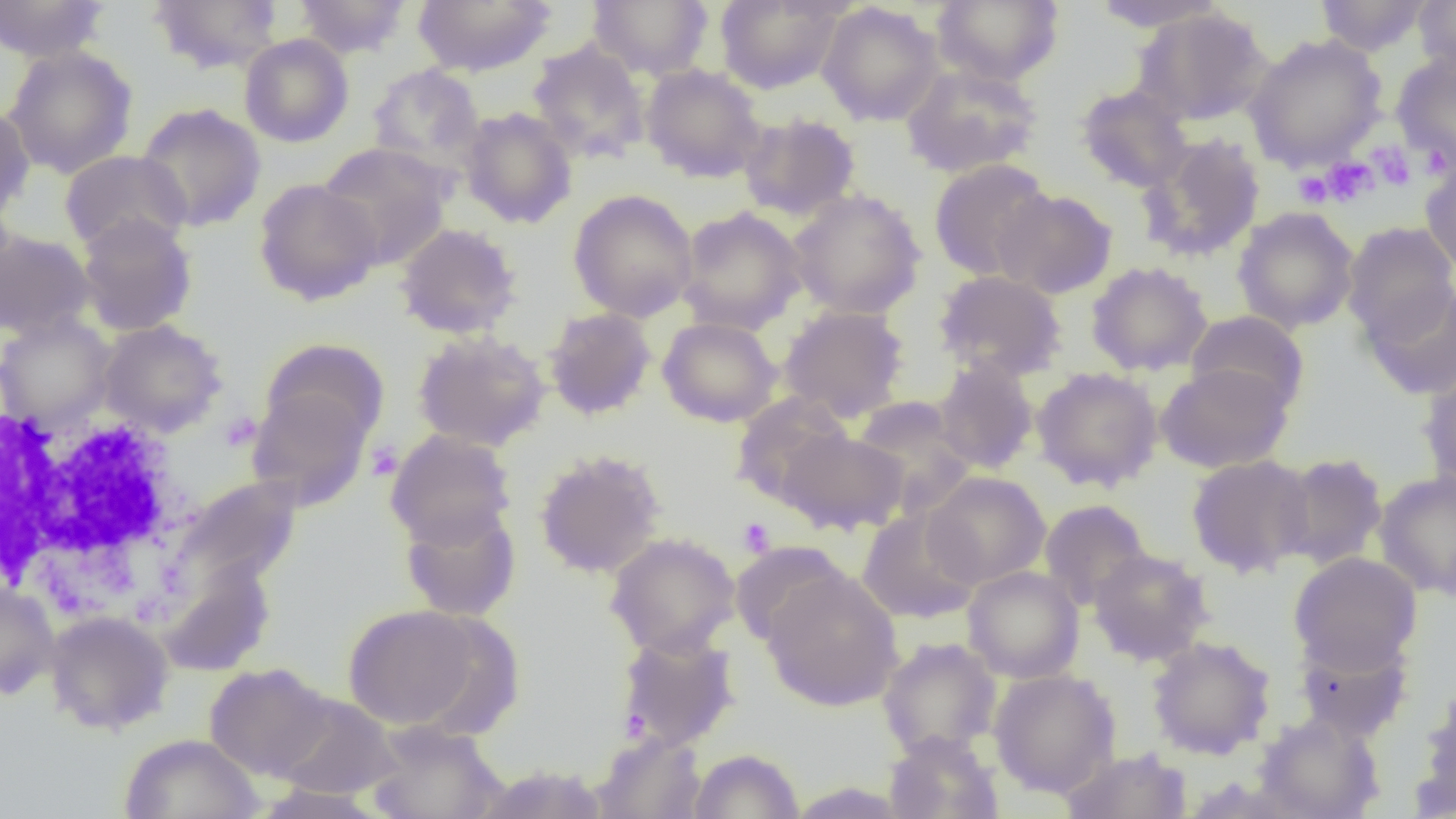

Summary:
  - Coordinate format: approximate bounding boxes as (x1,y1)-(x2,y2) corner pairs in pixels
  - Uninfected red blood cell locations: (0,0)-(110,62), (147,0)-(283,75), (293,0)-(412,59), (413,0)-(556,77), (587,0)-(714,80), (714,0)-(849,95), (931,0)-(1065,86), (1088,0)-(1228,32), (1313,0)-(1434,56), (1414,0)-(1456,79), (816,2)-(945,127), (1133,7)-(1273,127), (239,33)-(354,148), (1244,34)-(1387,171), (527,40)-(651,165), (2,45)-(139,179), (1391,54)-(1456,175), (366,64)-(486,177), (641,64)-(767,183), (900,64)-(1044,178), (1075,84)-(1194,193), (0,100)-(35,222), (135,102)-(267,233), (459,106)-(578,229), (738,113)-(861,220), (1138,133)-(1266,262), (316,142)-(454,270), (59,149)-(191,255), (1420,156)-(1456,277), (928,159)-(1052,281), (253,178)-(382,305), (568,188)-(699,322), (788,188)-(926,320), (992,188)-(1118,299), (676,205)-(807,335), (1232,206)-(1360,334), (75,213)-(198,336), (394,222)-(523,339), (1342,222)-(1456,346), (0,229)-(96,340), (1086,261)-(1213,377), (933,270)-(1067,382), (1362,283)-(1456,400), (778,305)-(910,423), (543,307)-(658,421), (1185,310)-(1309,412), (0,314)-(116,428), (657,316)-(782,427), (97,319)-(227,437), (412,330)-(551,451), (259,338)-(390,451), (932,359)-(1039,474), (1155,363)-(1294,473), (1418,363)-(1456,493), (1031,366)-(1164,492), (246,385)-(374,512), (730,393)-(853,509), (850,396)-(977,514), (384,429)-(517,549), (779,429)-(908,535), (534,448)-(667,580), (1275,452)-(1389,570), (1186,455)-(1314,578), (1374,470)-(1456,599), (923,471)-(1051,588), (171,476)-(303,597), (1039,499)-(1151,610), (399,502)-(522,621), (857,507)-(983,624), (604,532)-(741,659), (1088,547)-(1214,666), (1289,552)-(1422,673), (156,559)-(276,676), (963,565)-(1084,683), (976,566)-(1096,799), (761,568)-(904,712), (0,581)-(60,701), (342,603)-(491,732), (45,610)-(174,734), (614,630)-(742,754), (1293,630)-(1414,742), (1146,635)-(1276,759), (877,637)-(1002,759), (204,662)-(335,780), (988,668)-(1122,798), (1415,688)-(1456,815), (268,692)-(402,800), (1253,712)-(1385,819), (365,722)-(508,819), (590,731)-(708,818), (883,731)-(1004,819), (120,733)-(263,819), (1059,747)-(1193,819), (687,748)-(805,818), (469,763)-(612,819), (251,783)-(390,818)
  - Platelet locations: (1370,143)-(1416,190), (1322,157)-(1377,206), (1293,170)-(1333,207), (737,517)-(775,557)
  - White blood cell locations: (0,398)-(196,606)
  - Slide-level diagnosis: no evidence of blood parasites
  - Preparation: thin blood smear
  - Image size: 1456×819 pixels
  - Field of view: one of a larger specimen
  - Magnification: 1000x
  - Modality: optical microscopy